Give the preparation type.
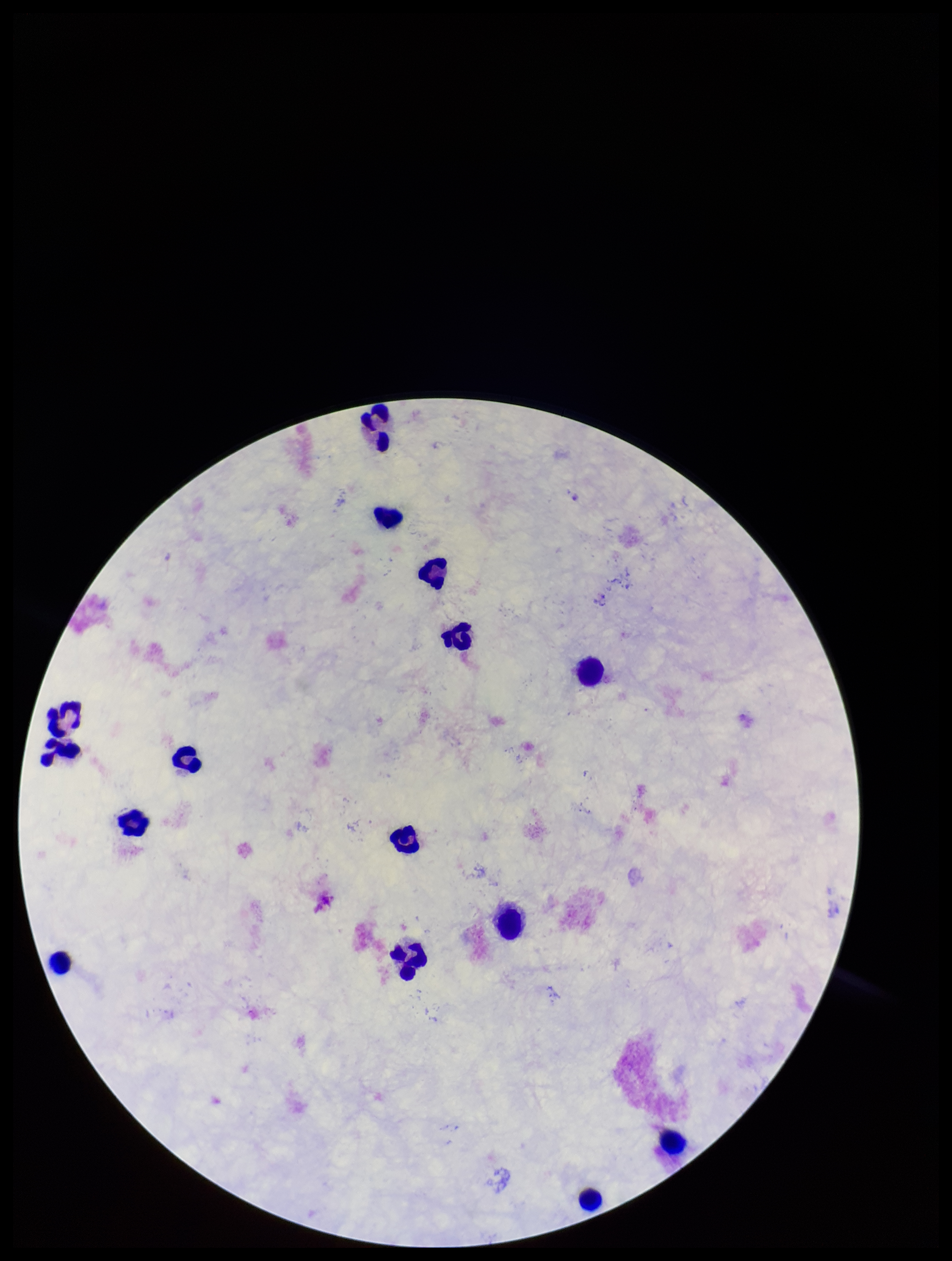
It is a thick blood smear.

Summary:
  - Leukocyte count: 15
  - Plasmodium parasites: none detected
  - Patient malaria status: negative
  - Field of view: one from this slide
  - Stain: Giemsa
  - Image size: 952×1261 pixels
  - Parasite count: 0
  - Capture: smartphone photograph through the microscope eyepiece